Report the malaria status of this cell.
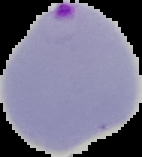
Parasitized.

image type = cell region segmented out of the field of view; surrounding area masked to black
preparation = thin blood film
image size = 142×157 pixels